Report the malaria status of this cell.
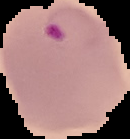

It is parasitized.

Summary:
  - Image size: 130×139 pixels
  - Preparation: thin blood smear
  - Image type: segmented cell region with the area outside set to black